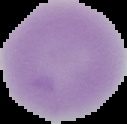
Cell region segmented out of the field of view; the surrounding area is masked to black. From a thin blood smear. Image is 127×124 pixels. Malaria status: uninfected.